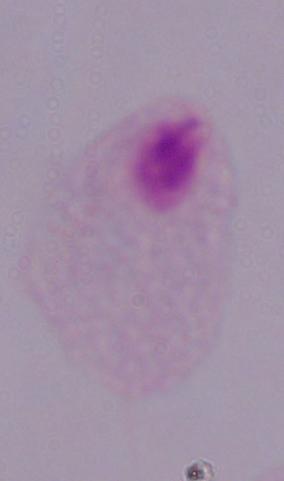
Summary:
  - Magnification: 1000x
  - Identification: trichomonad
  - Modality: micrograph